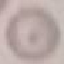
Result: no malaria parasites detected. Acquired by smartphone through the microscope eyepiece. Automatically extracted cell patch, resized to 64 × 64 pixels. Thin smear of blood. Giemsa stain.